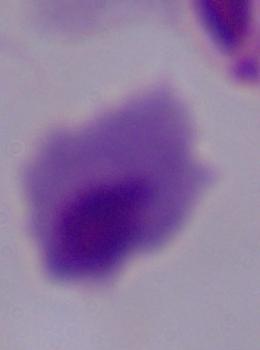

Summary:
  - Modality: micrograph
  - Magnification: 1000x
  - Identification: trichomonad